Give the preparation type.
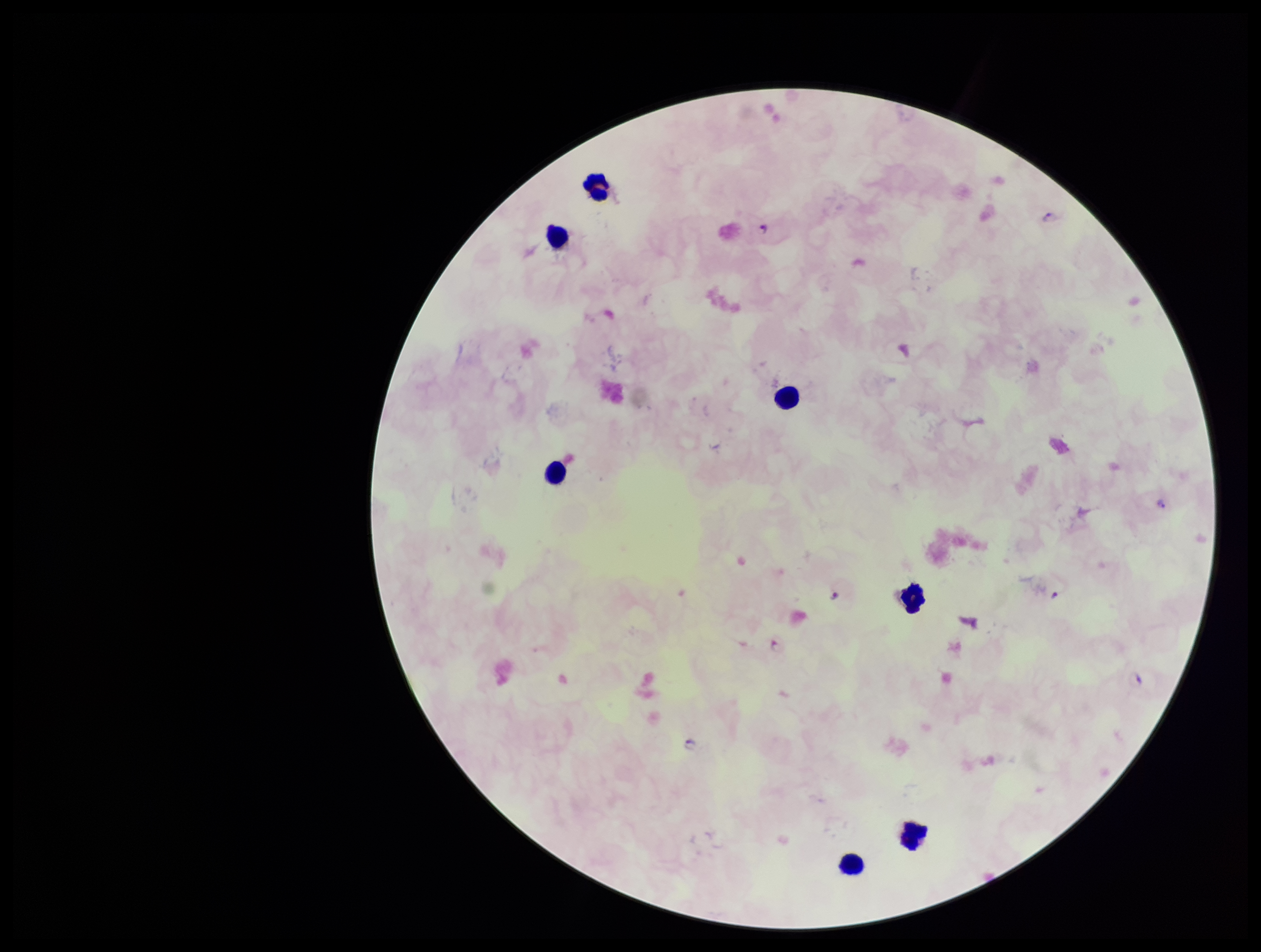

Thick.

Summary:
  - Patient malaria status: positive
  - Plasmodium parasites: identified
  - Species reported for this patient: Plasmodium falciparum
  - Capture: smartphone photograph through the microscope eyepiece
  - Field of view: single
  - Stain: Giemsa
  - Leukocyte count: 7
  - Image size: 1261×952 pixels
  - Parasite count: 5